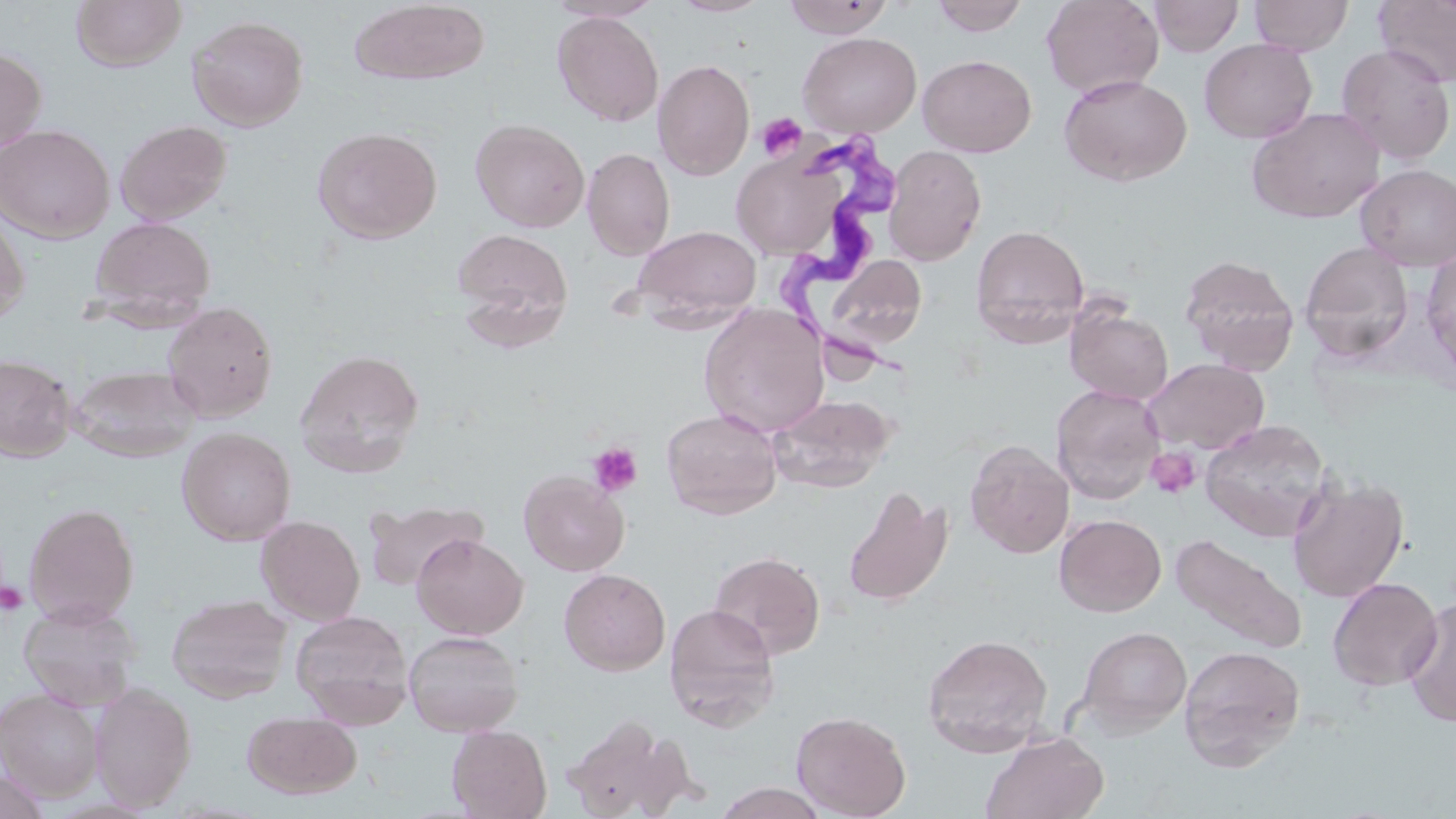 Approximate bounding boxes as named x1/y1/x2/y2 corners in pixels. Uninfected red blood cell locations: (x1=544, y1=0, x2=664, y2=22), (x1=669, y1=0, x2=774, y2=17), (x1=783, y1=0, x2=895, y2=38), (x1=930, y1=0, x2=1030, y2=36), (x1=1041, y1=0, x2=1164, y2=98), (x1=1149, y1=0, x2=1244, y2=57), (x1=1249, y1=0, x2=1353, y2=55), (x1=1374, y1=0, x2=1456, y2=88), (x1=70, y1=1, x2=187, y2=72), (x1=349, y1=2, x2=490, y2=85), (x1=552, y1=11, x2=664, y2=127), (x1=187, y1=14, x2=309, y2=131), (x1=798, y1=32, x2=922, y2=138), (x1=1199, y1=39, x2=1317, y2=143), (x1=1335, y1=44, x2=1454, y2=165), (x1=0, y1=46, x2=48, y2=157), (x1=917, y1=54, x2=1037, y2=157), (x1=652, y1=59, x2=755, y2=180), (x1=1059, y1=74, x2=1192, y2=187), (x1=1246, y1=107, x2=1386, y2=223), (x1=470, y1=117, x2=590, y2=232), (x1=115, y1=119, x2=233, y2=225), (x1=0, y1=124, x2=115, y2=243), (x1=311, y1=126, x2=442, y2=244), (x1=884, y1=145, x2=987, y2=265), (x1=582, y1=147, x2=675, y2=260), (x1=732, y1=148, x2=846, y2=260), (x1=1356, y1=163, x2=1456, y2=271), (x1=0, y1=207, x2=30, y2=326), (x1=89, y1=216, x2=215, y2=321), (x1=970, y1=224, x2=1090, y2=347), (x1=631, y1=225, x2=762, y2=325), (x1=451, y1=226, x2=574, y2=342), (x1=1299, y1=243, x2=1415, y2=362), (x1=1421, y1=247, x2=1456, y2=383), (x1=825, y1=254, x2=927, y2=354), (x1=1179, y1=254, x2=1300, y2=374), (x1=162, y1=301, x2=278, y2=421), (x1=1065, y1=303, x2=1174, y2=405), (x1=698, y1=304, x2=830, y2=438), (x1=294, y1=349, x2=426, y2=477), (x1=0, y1=353, x2=75, y2=461), (x1=1142, y1=358, x2=1269, y2=455), (x1=67, y1=364, x2=201, y2=462), (x1=1051, y1=384, x2=1165, y2=504), (x1=768, y1=393, x2=894, y2=493), (x1=661, y1=408, x2=783, y2=519), (x1=1200, y1=420, x2=1332, y2=541), (x1=176, y1=427, x2=296, y2=545), (x1=965, y1=439, x2=1074, y2=559), (x1=518, y1=470, x2=629, y2=576), (x1=1286, y1=475, x2=1409, y2=602), (x1=842, y1=484, x2=953, y2=607), (x1=363, y1=499, x2=488, y2=592), (x1=24, y1=502, x2=139, y2=626), (x1=1054, y1=513, x2=1166, y2=617), (x1=256, y1=515, x2=365, y2=625), (x1=1171, y1=532, x2=1308, y2=653), (x1=411, y1=533, x2=528, y2=639), (x1=708, y1=550, x2=826, y2=659), (x1=559, y1=568, x2=671, y2=675), (x1=1327, y1=576, x2=1443, y2=691), (x1=167, y1=593, x2=293, y2=703), (x1=1400, y1=598, x2=1456, y2=728), (x1=19, y1=600, x2=142, y2=711), (x1=663, y1=603, x2=781, y2=731), (x1=291, y1=610, x2=414, y2=728), (x1=1076, y1=625, x2=1192, y2=736), (x1=404, y1=630, x2=523, y2=736), (x1=921, y1=633, x2=1054, y2=757), (x1=1178, y1=644, x2=1306, y2=771), (x1=89, y1=683, x2=196, y2=811), (x1=1, y1=688, x2=104, y2=801), (x1=242, y1=710, x2=361, y2=799), (x1=791, y1=710, x2=911, y2=819), (x1=559, y1=715, x2=692, y2=819), (x1=447, y1=724, x2=552, y2=819), (x1=980, y1=731, x2=1109, y2=819), (x1=0, y1=770, x2=51, y2=819), (x1=712, y1=783, x2=830, y2=818). Platelet locations: (x1=756, y1=113, x2=807, y2=161), (x1=587, y1=442, x2=643, y2=497), (x1=1146, y1=446, x2=1200, y2=500), (x1=0, y1=581, x2=28, y2=616). Trypanosoma brucei locations: (x1=779, y1=133, x2=917, y2=383). Slide-level diagnosis: Trypanosoma brucei. Captured at 1000x magnification. Thin blood smear. Light microscopy. May-Grünwald-Giemsa-stained preparation. Single field of view. Image is 1456×819 pixels.